Give the extent of all Plasmodium vivax-infected red blood cells.
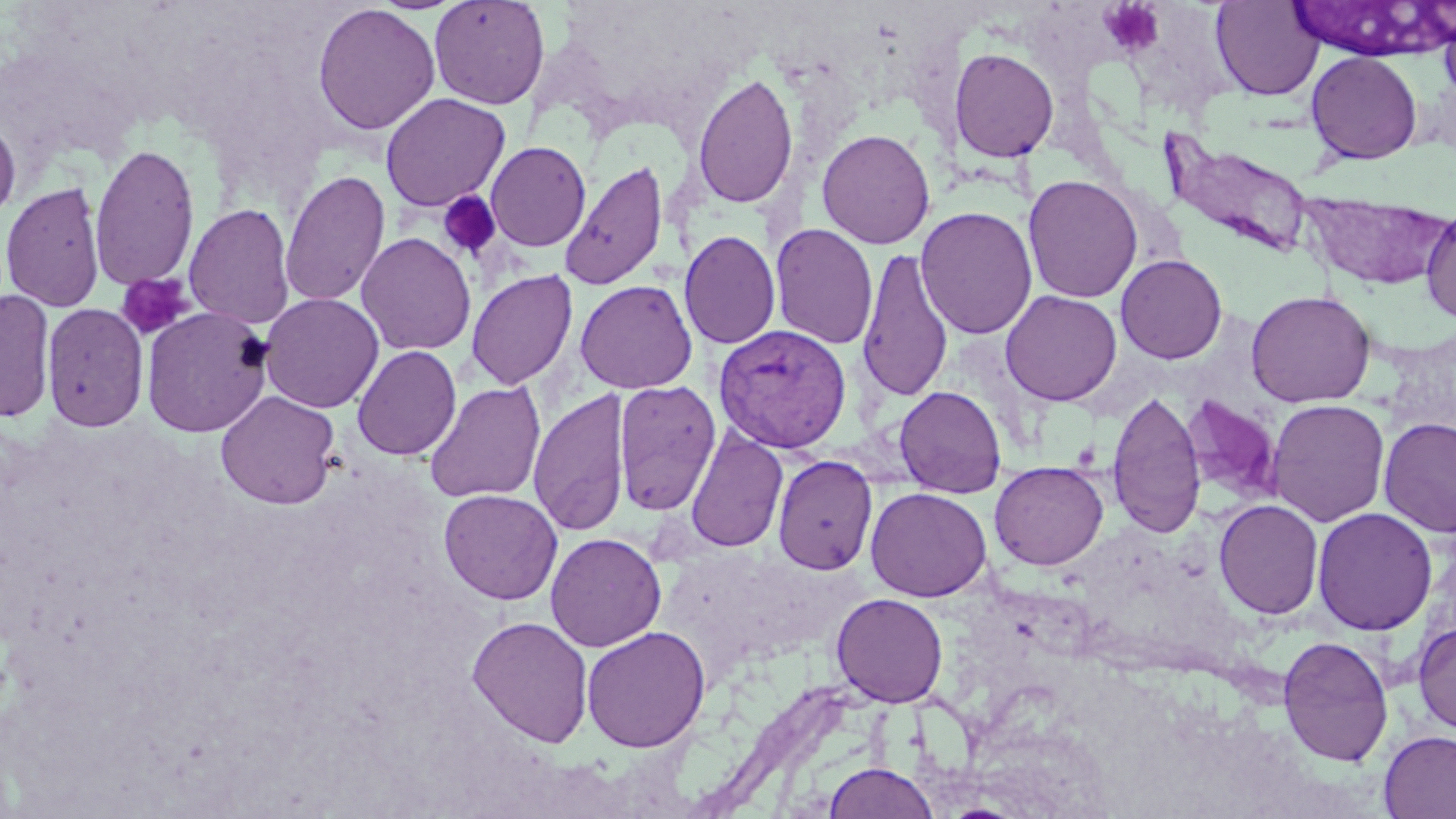

Approximate bounding boxes as named x1/y1/x2/y2 corners in pixels.
Plasmodium vivax-infected red blood cells: (x1=712, y1=323, x2=852, y2=453).

Summary:
  - Uninfected red blood cell locations: (x1=429, y1=0, x2=550, y2=110), (x1=1210, y1=1, x2=1325, y2=101), (x1=1292, y1=1, x2=1443, y2=61), (x1=312, y1=3, x2=441, y2=136), (x1=1438, y1=7, x2=1456, y2=110), (x1=949, y1=47, x2=1060, y2=162), (x1=1305, y1=51, x2=1422, y2=164), (x1=692, y1=70, x2=799, y2=210), (x1=380, y1=92, x2=510, y2=212), (x1=0, y1=115, x2=21, y2=225), (x1=816, y1=128, x2=936, y2=249), (x1=1165, y1=138, x2=1315, y2=258), (x1=485, y1=141, x2=591, y2=251), (x1=90, y1=142, x2=200, y2=291), (x1=560, y1=159, x2=668, y2=291), (x1=279, y1=170, x2=390, y2=308), (x1=1023, y1=174, x2=1143, y2=303), (x1=1, y1=181, x2=105, y2=312), (x1=1299, y1=192, x2=1456, y2=291), (x1=185, y1=202, x2=295, y2=329), (x1=916, y1=206, x2=1038, y2=339), (x1=1420, y1=208, x2=1456, y2=325), (x1=769, y1=222, x2=878, y2=349), (x1=679, y1=230, x2=781, y2=350), (x1=356, y1=232, x2=476, y2=356), (x1=857, y1=249, x2=954, y2=403), (x1=1115, y1=254, x2=1227, y2=364), (x1=466, y1=269, x2=578, y2=390), (x1=574, y1=279, x2=698, y2=394), (x1=0, y1=289, x2=55, y2=423), (x1=1000, y1=290, x2=1122, y2=406), (x1=1246, y1=290, x2=1376, y2=408), (x1=259, y1=293, x2=384, y2=413), (x1=42, y1=301, x2=149, y2=432), (x1=141, y1=306, x2=274, y2=437), (x1=352, y1=345, x2=461, y2=461), (x1=424, y1=380, x2=546, y2=504), (x1=613, y1=380, x2=721, y2=515), (x1=894, y1=385, x2=1007, y2=498), (x1=528, y1=388, x2=631, y2=537), (x1=215, y1=390, x2=341, y2=509), (x1=1106, y1=390, x2=1206, y2=539), (x1=1180, y1=394, x2=1282, y2=505), (x1=1266, y1=399, x2=1390, y2=526), (x1=1377, y1=417, x2=1456, y2=538), (x1=685, y1=429, x2=788, y2=553), (x1=772, y1=454, x2=878, y2=575), (x1=989, y1=461, x2=1108, y2=570), (x1=865, y1=487, x2=992, y2=602), (x1=438, y1=488, x2=562, y2=605), (x1=1213, y1=499, x2=1324, y2=619), (x1=1312, y1=507, x2=1437, y2=635), (x1=545, y1=532, x2=666, y2=652), (x1=830, y1=592, x2=949, y2=707), (x1=466, y1=615, x2=594, y2=747), (x1=1412, y1=621, x2=1456, y2=735), (x1=581, y1=625, x2=711, y2=752), (x1=1277, y1=635, x2=1394, y2=767), (x1=1378, y1=729, x2=1456, y2=819), (x1=824, y1=761, x2=939, y2=819)
  - Platelet locations: (x1=1099, y1=0, x2=1166, y2=57), (x1=437, y1=191, x2=501, y2=261), (x1=117, y1=273, x2=195, y2=340), (x1=1071, y1=439, x2=1102, y2=471)
  - Slide-level diagnosis: Plasmodium vivax
  - Magnification: 1000x
  - Preparation: thin blood film
  - Modality: optical microscopy
  - Field of view: single
  - Stain: May-Grünwald-Giemsa
  - Image size: 1456×819 pixels